Classify this cell by malaria status.
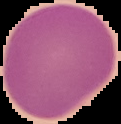

Uninfected.

image type = segmented cell region with the area outside set to black
image size = 121×124 pixels
preparation = thin blood film